Assess the morphology of the red blood cells.
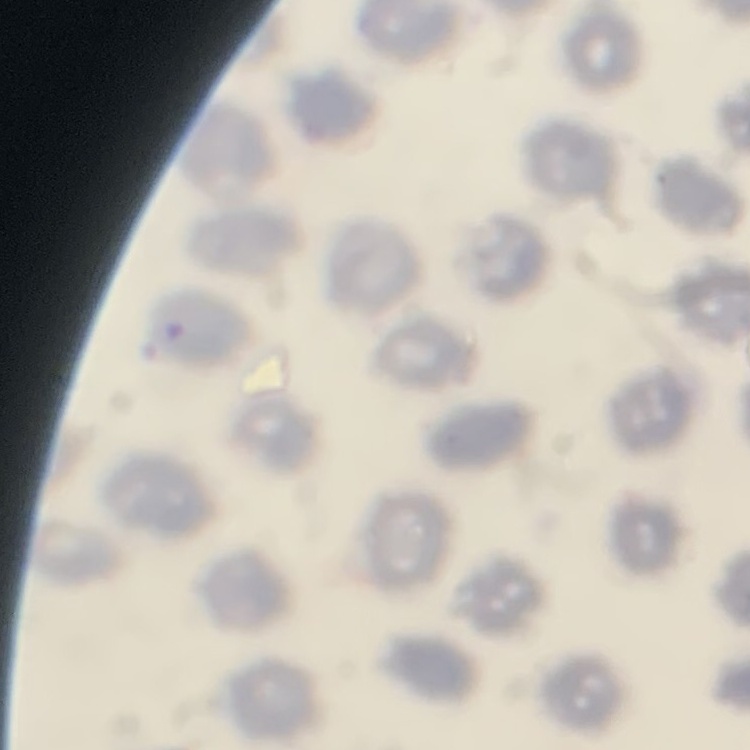

No rouleaux formation.

image type = one tile cut from a larger photomicrograph
preparation = thin peripheral smear
stain = Field's or Giemsa